Identify the cell.
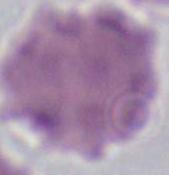
An erythrocyte.

magnification = 1000x
modality = micrograph